Name the blood parasite species.
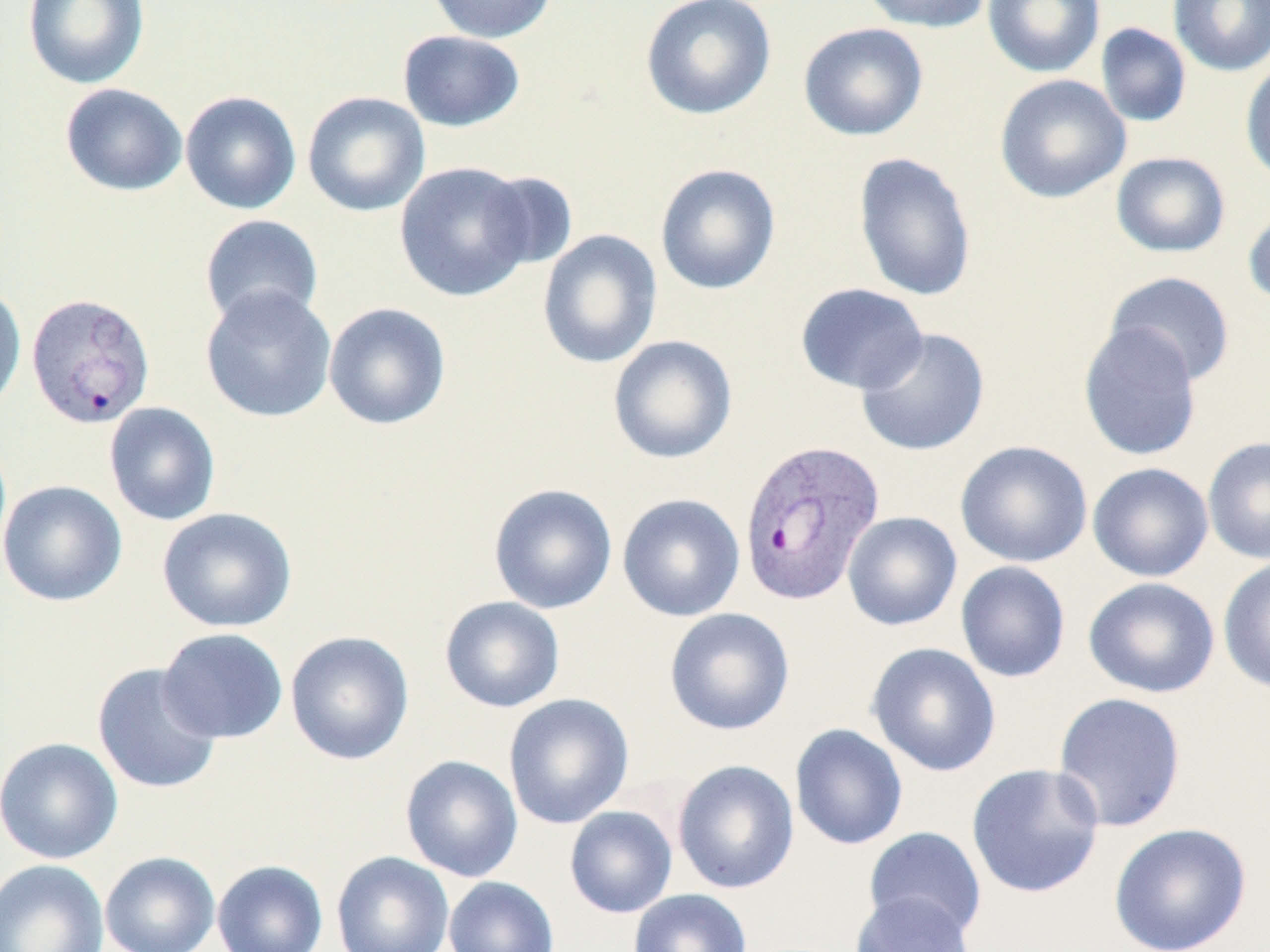
Plasmodium vivax.

Approximate bounding boxes as named x1/y1/x2/y2 corners in pixels. Plasmodium vivax-infected red blood cell locations: (x1=26, y1=292, x2=156, y2=430), (x1=737, y1=436, x2=886, y2=605). Uninfected red blood cell locations: (x1=22, y1=0, x2=150, y2=90), (x1=424, y1=0, x2=559, y2=44), (x1=640, y1=0, x2=777, y2=120), (x1=857, y1=0, x2=995, y2=33), (x1=983, y1=0, x2=1105, y2=78), (x1=1168, y1=0, x2=1270, y2=77), (x1=798, y1=22, x2=929, y2=141), (x1=1095, y1=22, x2=1192, y2=128), (x1=397, y1=30, x2=526, y2=132), (x1=1240, y1=57, x2=1270, y2=188), (x1=994, y1=74, x2=1131, y2=204), (x1=60, y1=83, x2=188, y2=197), (x1=180, y1=91, x2=302, y2=215), (x1=302, y1=91, x2=430, y2=217), (x1=1111, y1=151, x2=1231, y2=258), (x1=852, y1=152, x2=977, y2=302), (x1=394, y1=161, x2=537, y2=302), (x1=655, y1=163, x2=781, y2=295), (x1=478, y1=171, x2=578, y2=272), (x1=1243, y1=202, x2=1270, y2=310), (x1=199, y1=215, x2=323, y2=329), (x1=537, y1=229, x2=663, y2=369), (x1=1104, y1=271, x2=1236, y2=387), (x1=0, y1=283, x2=27, y2=416), (x1=795, y1=283, x2=929, y2=395), (x1=199, y1=285, x2=337, y2=423), (x1=323, y1=302, x2=451, y2=430), (x1=1077, y1=321, x2=1203, y2=462), (x1=855, y1=327, x2=990, y2=457), (x1=607, y1=335, x2=738, y2=464), (x1=103, y1=401, x2=221, y2=525), (x1=1202, y1=435, x2=1270, y2=565), (x1=955, y1=440, x2=1093, y2=568), (x1=1087, y1=462, x2=1214, y2=582), (x1=0, y1=480, x2=127, y2=606), (x1=488, y1=483, x2=618, y2=614), (x1=617, y1=493, x2=745, y2=622), (x1=156, y1=506, x2=297, y2=633), (x1=842, y1=511, x2=962, y2=630), (x1=1218, y1=556, x2=1270, y2=695), (x1=955, y1=560, x2=1070, y2=683), (x1=1082, y1=577, x2=1220, y2=699), (x1=439, y1=596, x2=566, y2=713), (x1=664, y1=607, x2=795, y2=735), (x1=157, y1=627, x2=288, y2=744), (x1=285, y1=630, x2=415, y2=766), (x1=866, y1=641, x2=1002, y2=776), (x1=92, y1=662, x2=223, y2=794), (x1=1052, y1=691, x2=1187, y2=833), (x1=503, y1=693, x2=635, y2=830), (x1=789, y1=723, x2=908, y2=850), (x1=0, y1=736, x2=123, y2=865), (x1=400, y1=755, x2=523, y2=882), (x1=672, y1=759, x2=799, y2=894), (x1=966, y1=763, x2=1105, y2=898), (x1=564, y1=806, x2=677, y2=918), (x1=1108, y1=822, x2=1252, y2=952), (x1=864, y1=826, x2=987, y2=940), (x1=100, y1=851, x2=220, y2=952), (x1=331, y1=851, x2=455, y2=952), (x1=0, y1=858, x2=109, y2=952), (x1=212, y1=859, x2=328, y2=952), (x1=443, y1=876, x2=560, y2=952), (x1=629, y1=889, x2=752, y2=952), (x1=850, y1=891, x2=977, y2=952). Thin blood film. Light microscopy. Image is 1270×952 pixels. Captured at 1000x magnification. May-Grünwald-Giemsa stain. Single field of view.